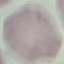
result = no malaria parasites detected
stain = Giemsa
preparation = thin blood film
capture = smartphone through the microscope eyepiece
image type = cell patch, automatically extracted from a larger field of view and resized to 64 × 64 pixels